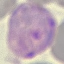

{
  "result": "malaria parasites detected",
  "capture": "smartphone through the microscope eyepiece",
  "stain": "Giemsa",
  "image_type": "cell patch, automatically extracted from a larger field of view and resized to 64 × 64 pixels",
  "preparation": "thin blood film"
}